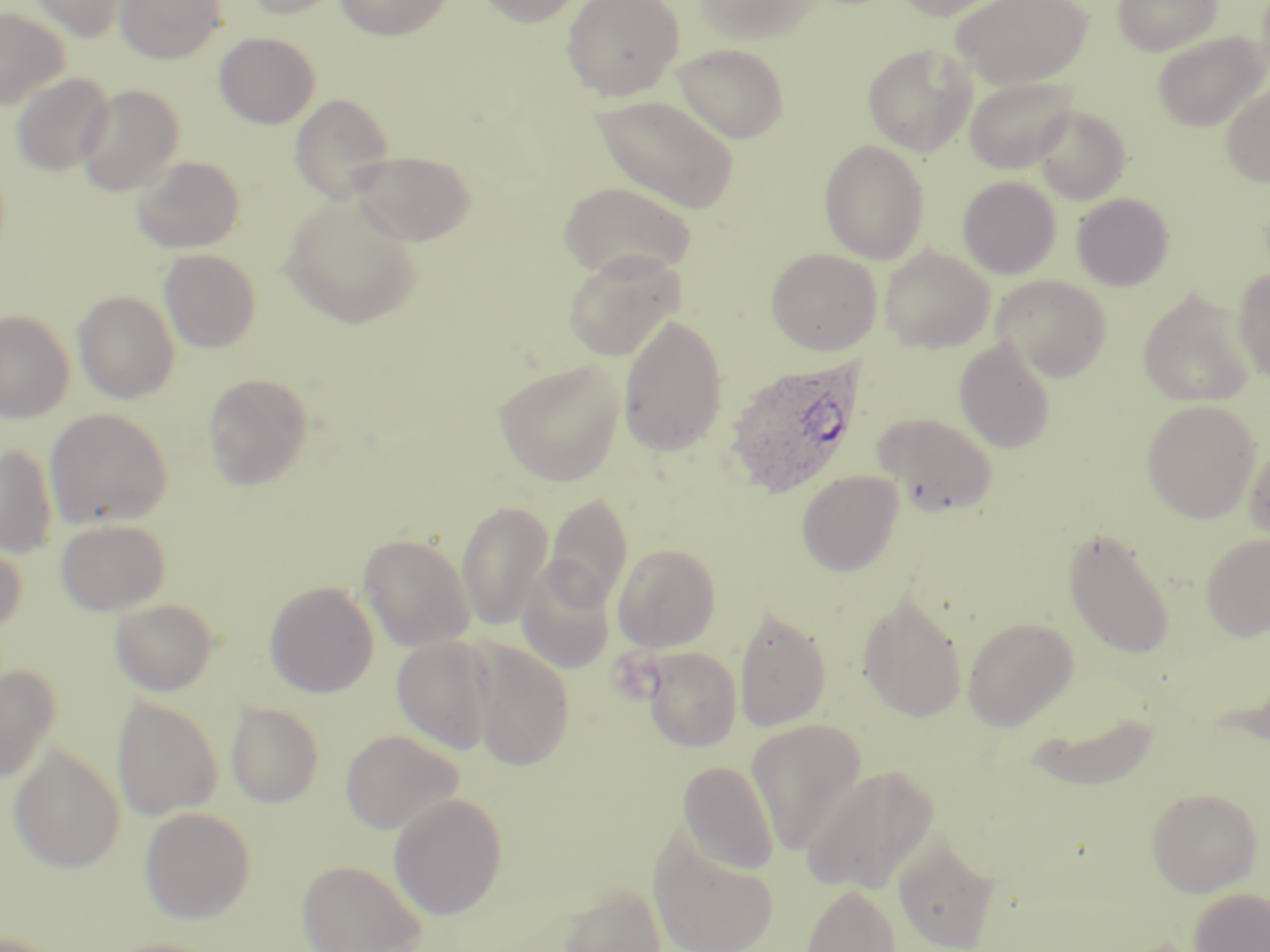

Approximate bounding boxes as [x1, y1, x2, y2] in pixels. Uninfected red blood cell locations: [27, 0, 129, 41], [115, 0, 227, 64], [239, 0, 346, 19], [334, 0, 452, 40], [475, 0, 584, 27], [561, 0, 685, 100], [696, 0, 825, 46], [890, 0, 1023, 21], [951, 0, 1093, 88], [1113, 0, 1220, 56], [0, 7, 69, 110], [1153, 31, 1268, 132], [214, 32, 320, 128], [671, 42, 790, 143], [863, 43, 976, 157], [11, 72, 114, 176], [964, 75, 1078, 174], [1220, 82, 1270, 187], [75, 84, 184, 197], [290, 93, 395, 202], [590, 93, 739, 214], [1033, 104, 1131, 205], [819, 139, 930, 264], [349, 149, 477, 246], [132, 155, 245, 253], [958, 175, 1061, 279], [558, 180, 696, 282], [1071, 193, 1174, 290], [281, 197, 423, 331], [879, 246, 994, 352], [159, 248, 261, 352], [766, 248, 881, 355], [563, 251, 686, 362], [1233, 268, 1270, 383], [992, 276, 1112, 382], [1137, 289, 1257, 407], [73, 290, 180, 404], [0, 309, 75, 424], [618, 314, 728, 456], [954, 339, 1056, 454], [494, 359, 625, 487], [202, 373, 313, 490], [1141, 399, 1261, 522], [44, 408, 174, 529], [873, 412, 998, 516], [1244, 438, 1270, 544], [0, 442, 59, 558], [797, 470, 904, 576], [544, 494, 633, 608], [457, 500, 553, 631], [55, 518, 170, 615], [1062, 526, 1176, 660], [358, 533, 475, 652], [1199, 534, 1270, 642], [0, 537, 28, 637], [613, 543, 721, 652], [516, 557, 617, 674], [264, 581, 379, 698], [858, 591, 968, 723], [110, 598, 218, 696], [734, 606, 832, 732], [962, 616, 1078, 730], [391, 636, 497, 754], [468, 640, 574, 772], [642, 647, 742, 751], [0, 664, 61, 784], [111, 695, 222, 821], [226, 701, 324, 808], [1020, 708, 1162, 791], [746, 719, 867, 854], [340, 729, 463, 835], [8, 743, 125, 873], [677, 760, 780, 875], [802, 763, 940, 895], [1145, 787, 1262, 897], [388, 792, 508, 919], [139, 806, 256, 923], [649, 831, 779, 952], [893, 834, 1001, 952], [297, 859, 426, 952], [556, 882, 666, 952], [800, 883, 902, 952], [1188, 888, 1270, 952], [98, 938, 226, 952]. Plasmodium ovale-infected red blood cell locations: [725, 357, 867, 498]. Slide-level diagnosis: Plasmodium ovale. May-Grünwald-Giemsa stain. One field of a larger specimen. Image is 1270×952 pixels. Light microscopy. Thin blood film. Captured at 1000x magnification.